Identify the parasite.
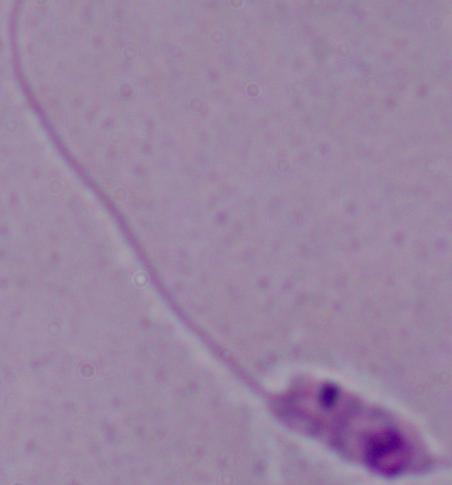

This is Leishmania.

Captured at 1000x magnification. Micrograph.